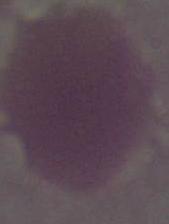
An erythrocyte is shown. Photomicrograph. Captured at 1000x magnification.